Point out each leukocyte.
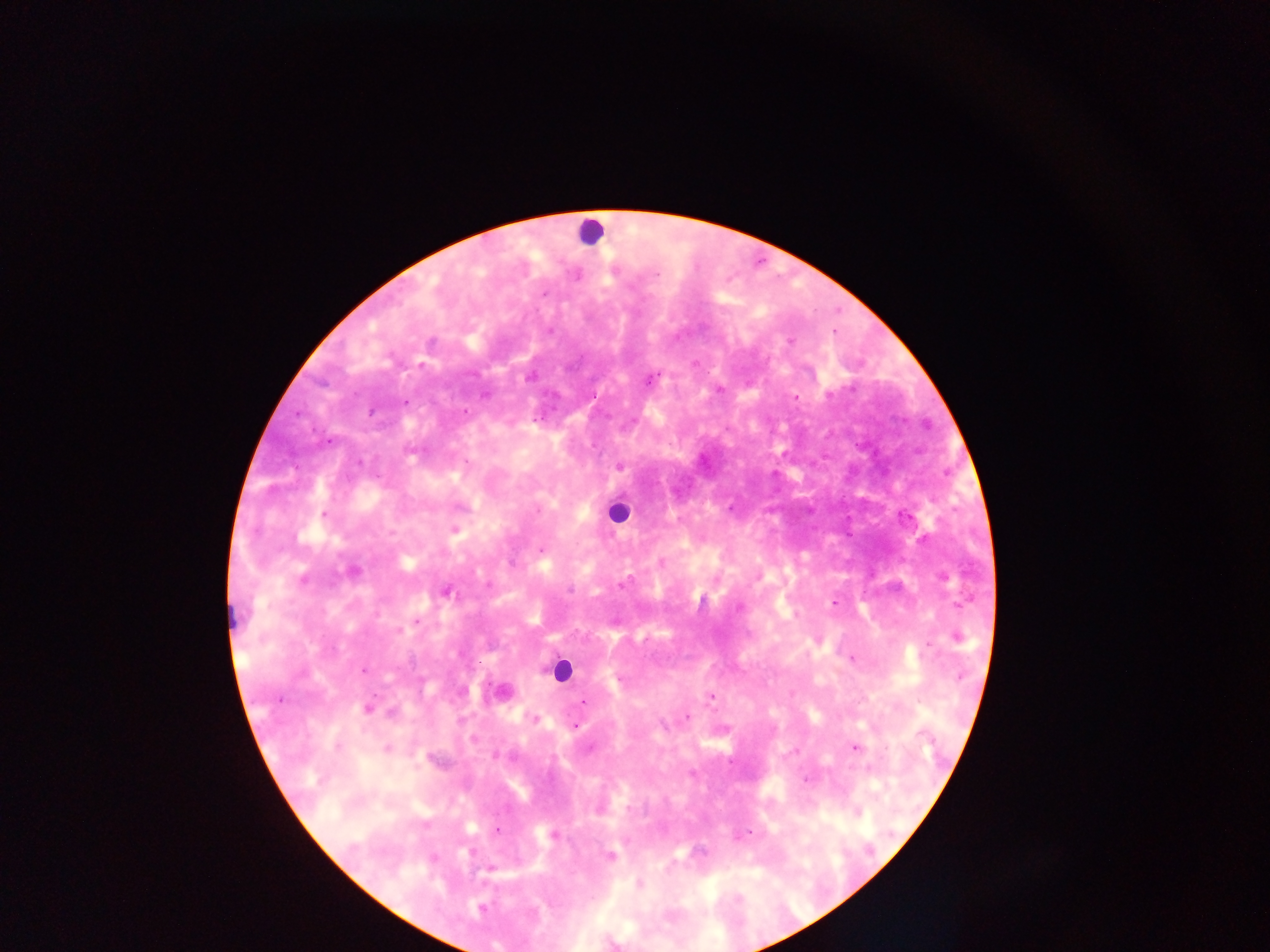
Approximate centers as {x, y} in pixels.
Leukocytes: {590, 233}, {618, 512}, {231, 617}, {560, 670}, {500, 692}.

Malaria parasite locations: {790, 341}, {530, 375}, {650, 377}, {718, 390}, {405, 402}, {619, 467}, {323, 515}, {455, 529}, {541, 549}, {661, 562}, {352, 571}, {446, 591}, {834, 602}, {739, 607}, {955, 637}, {852, 658}, {711, 695}, {279, 699}, {583, 702}, {367, 708}, {686, 717}, {533, 719}, {575, 725}, {855, 748}, {386, 749}, {806, 779}, {599, 807}, {857, 812}, {496, 830}, {553, 835}, {740, 835}, {609, 856}, {638, 884}, {480, 908}. Thick blood film. Image is 1270×952 pixels. Single field of view. Sample from Ghana. Photographed through a microscope with a mobile-phone camera.